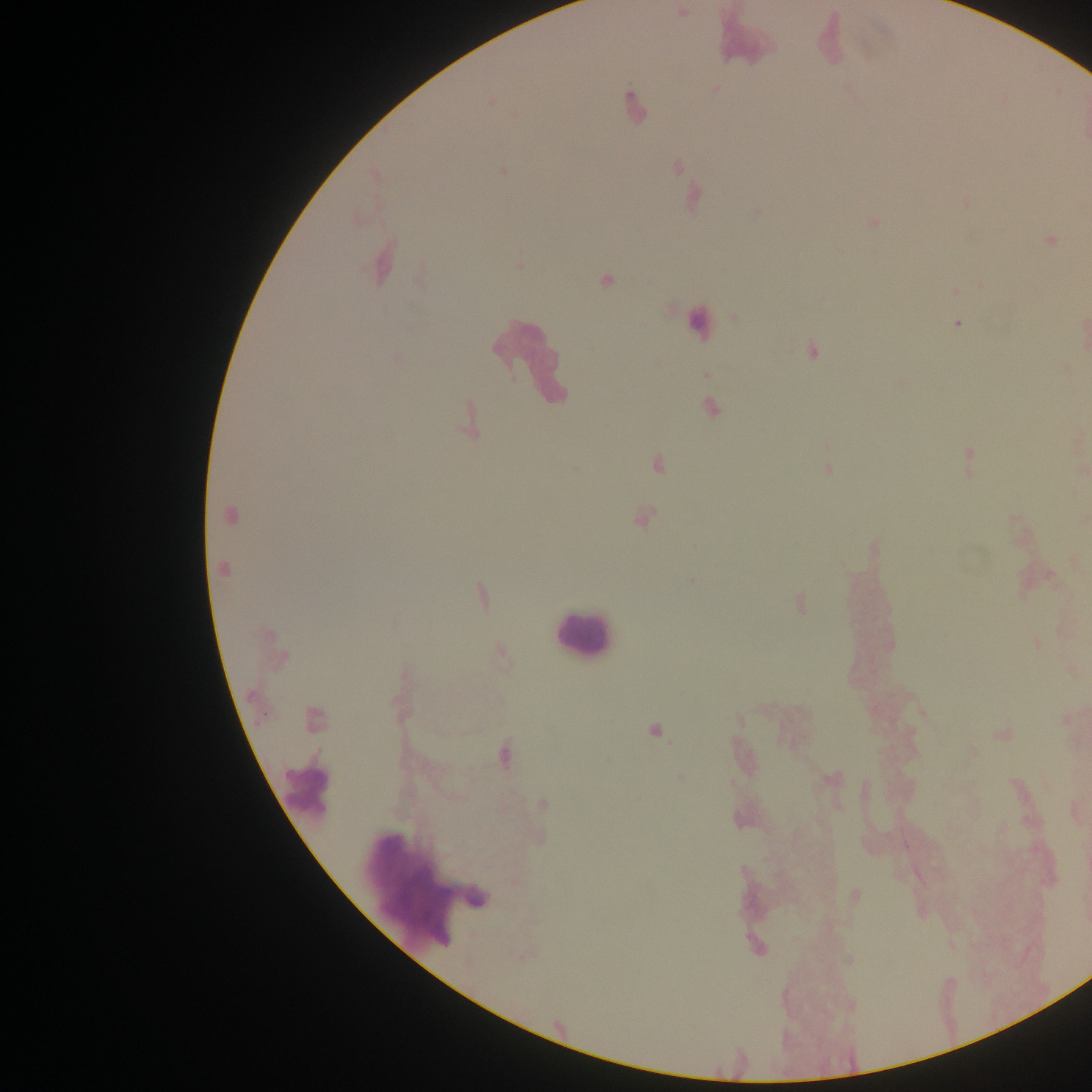
Plasmodium parasite locations = approximate centers as [x, y] in pixels: [491, 102], [633, 105], [502, 171], [1051, 241], [605, 281], [957, 324], [813, 350], [711, 408], [969, 461], [657, 463], [828, 470], [230, 515], [643, 517], [223, 569], [691, 580], [481, 597], [800, 602], [1038, 643], [654, 731], [503, 754], [681, 779], [542, 804], [1002, 829], [742, 870]
leukocyte locations = approximate centers as [x, y] in pixels: [699, 323], [530, 357], [581, 634], [306, 792], [424, 879]
capture = mobile-phone photograph through a microscope
country = Ghana
preparation = thick blood smear
image size = 1092×1092 pixels
field of view = single